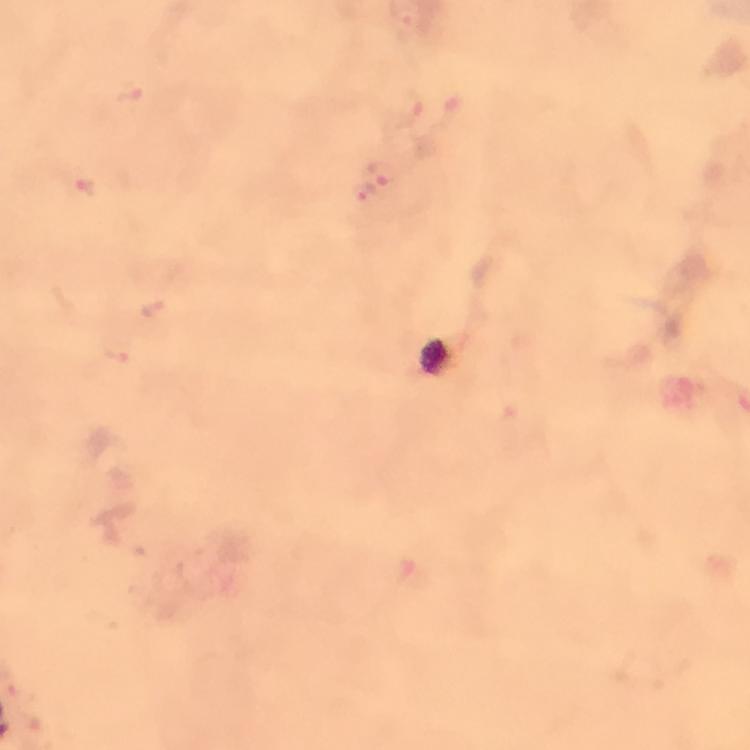

cropped from = one field of view
image size = 750×750 pixels
context = from a diagnostic examination for malaria
stain = Giemsa
magnification = 100x
preparation = thick smear
capture = smartphone camera through the microscope
malaria parasite locations = approximate centers as (x, y) in pixels: (130, 93), (407, 109), (384, 172), (88, 186), (368, 191), (154, 308), (116, 356)
immersion oil = used